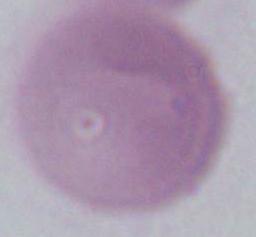
An erythrocyte is shown. Photomicrograph. Captured at 1000x magnification.